Identify the parasite.
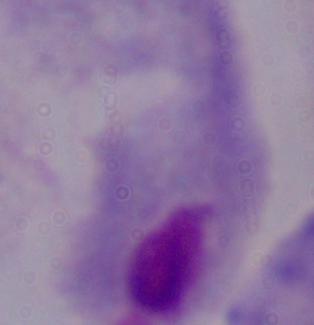

This is a trichomonad.

{
  "modality": "photomicrograph",
  "magnification": "1000x"
}